Name the cell type shown.
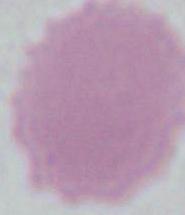

This is an erythrocyte.

{
  "modality": "photomicrograph",
  "magnification": "1000x"
}